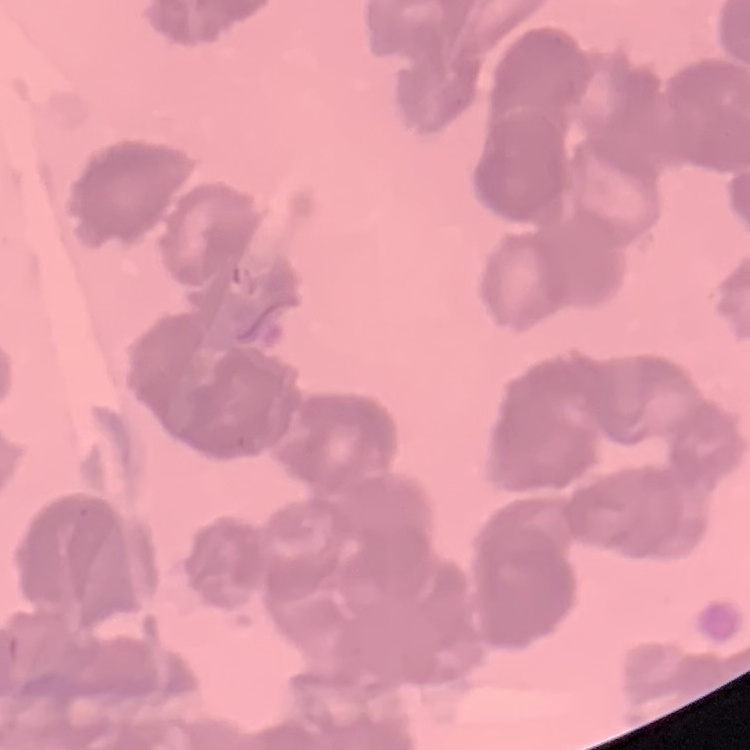 The erythrocytes show rouleaux formation. Stained with either Field's or Giemsa. Thin peripheral smear. Square crop of a larger photomicrograph.